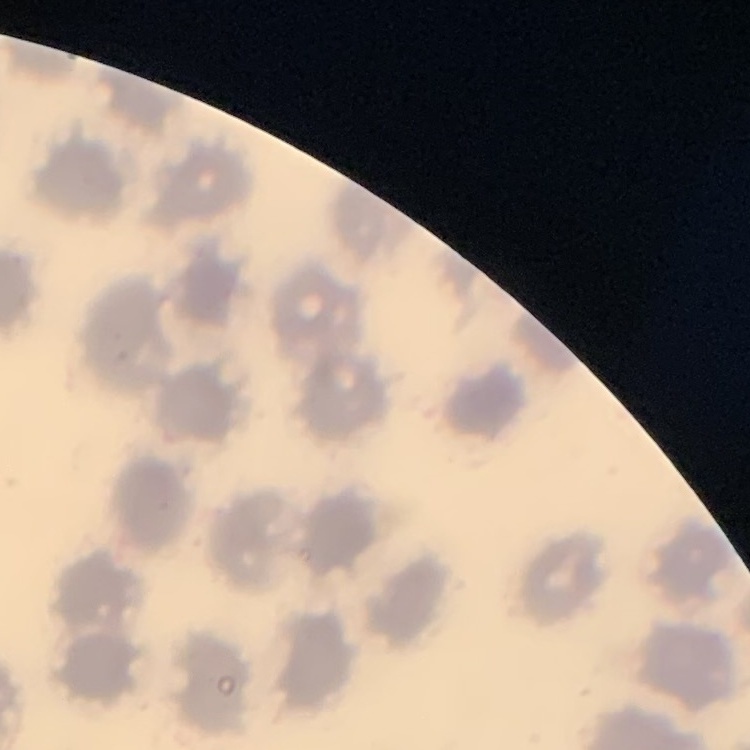 The red blood cells show no rouleaux formation. Field's or Giemsa stain. One tile cut from a larger photomicrograph. Thin blood film.